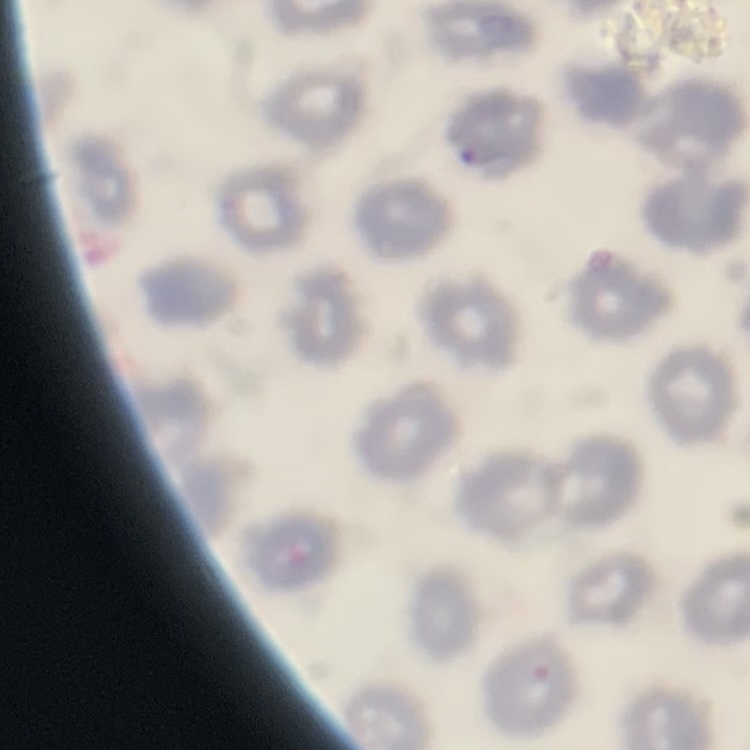
erythrocyte morphology = no rouleaux formation
stain = Field's or Giemsa
preparation = thin blood film
image type = square crop of a larger photomicrograph